Describe the morphology of the erythrocytes.
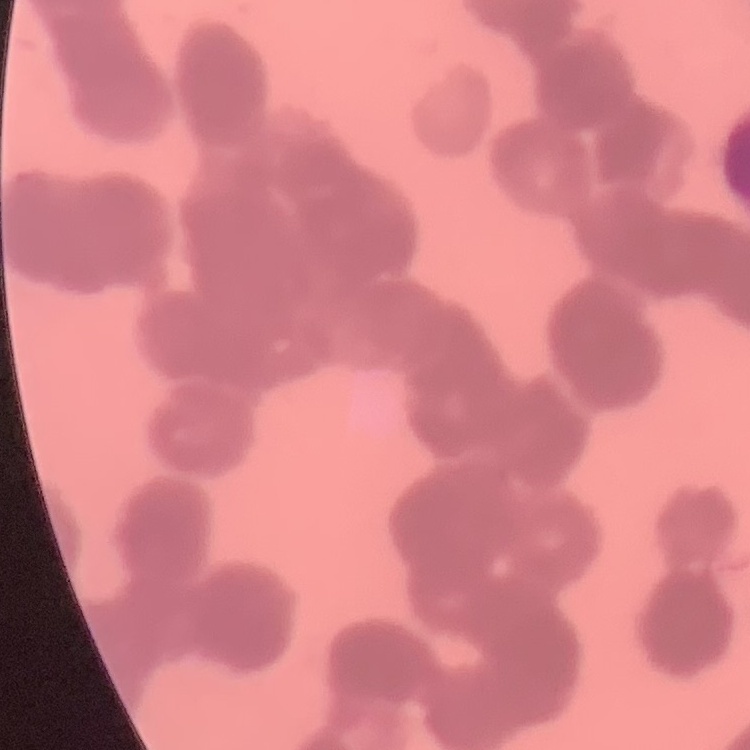
Rouleaux formation.

Stained with either Field's or Giemsa. Thin blood smear. Square crop of a larger photomicrograph.